Assess the morphology of the red blood cells.
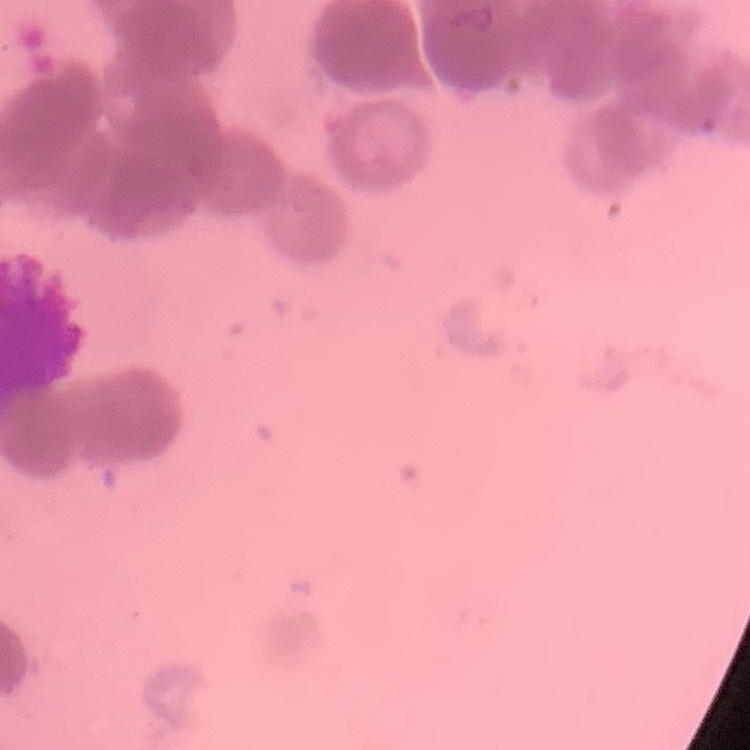

Rouleaux formation.

Summary:
  - Image type: square crop of a larger photomicrograph
  - Preparation: thin peripheral smear
  - Stain: Field's or Giemsa